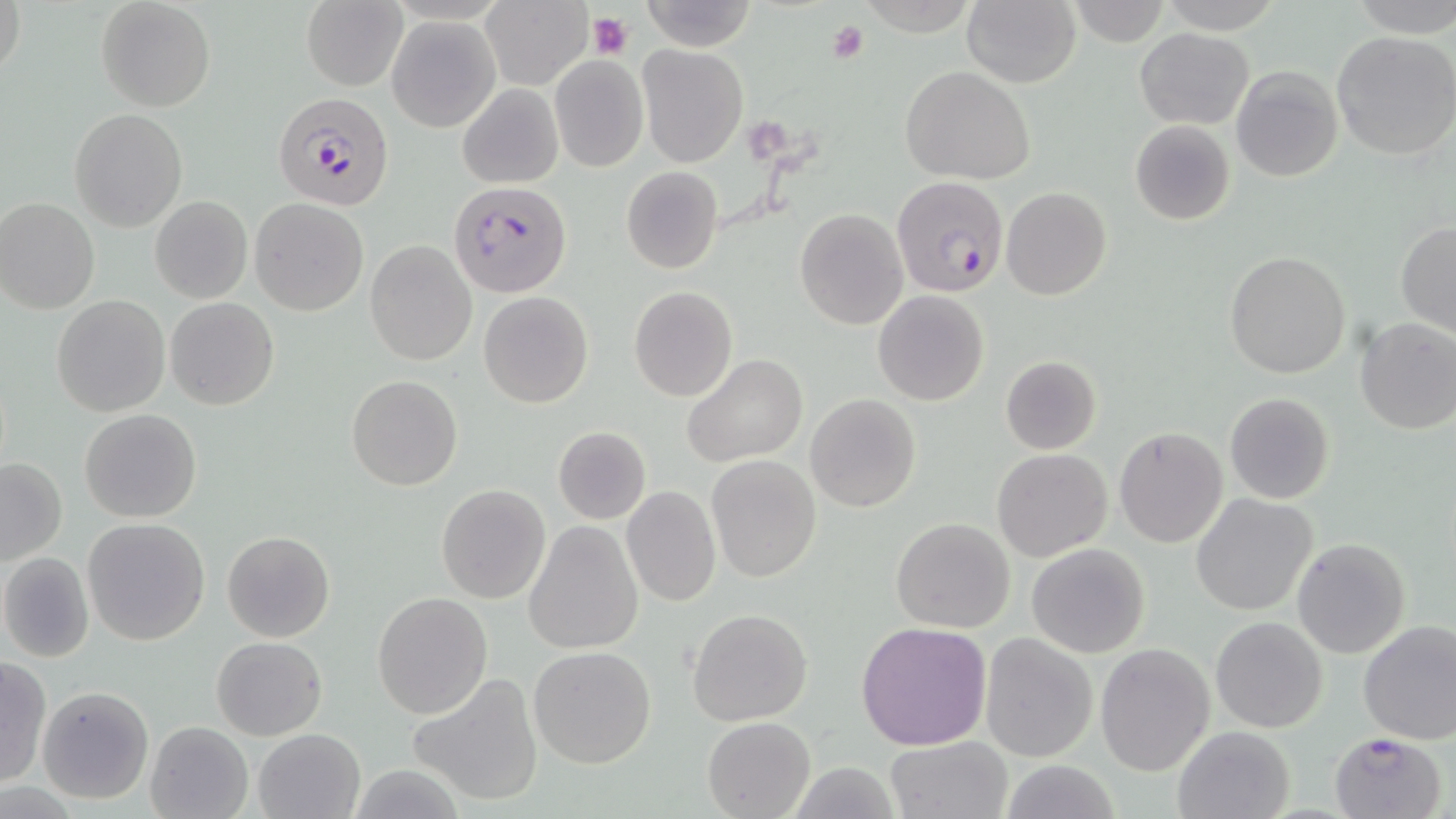

Summary:
  - Coordinate format: approximate bounding boxes as [x1, y1, x2, y2] in pixels
  - Uninfected red blood cell locations: [1, 0, 24, 85], [95, 0, 215, 112], [301, 0, 409, 91], [481, 0, 594, 90], [638, 0, 758, 51], [962, 0, 1081, 88], [1349, 0, 1456, 36], [1067, 1, 1171, 47], [389, 17, 499, 131], [1135, 28, 1254, 128], [1332, 31, 1456, 160], [638, 43, 748, 168], [549, 55, 648, 172], [902, 66, 1037, 185], [1231, 66, 1342, 183], [457, 84, 563, 188], [69, 109, 187, 232], [1130, 120, 1235, 225], [620, 166, 723, 274], [1001, 186, 1112, 300], [150, 195, 252, 303], [0, 197, 100, 314], [249, 198, 369, 316], [794, 208, 908, 330], [1396, 221, 1456, 335], [365, 240, 476, 365], [1225, 251, 1351, 377], [629, 286, 737, 401], [872, 290, 990, 406], [479, 292, 593, 408], [51, 294, 170, 417], [167, 298, 279, 411], [1355, 317, 1456, 435], [682, 354, 808, 467], [999, 356, 1102, 454], [347, 375, 461, 490], [1224, 393, 1334, 505], [806, 394, 921, 512], [79, 409, 202, 523], [552, 426, 652, 525], [1114, 428, 1227, 548], [992, 447, 1113, 562], [706, 455, 822, 584], [0, 457, 67, 565], [436, 484, 551, 603], [621, 485, 721, 607], [1191, 493, 1318, 615], [82, 518, 211, 646], [891, 518, 1015, 633], [523, 521, 643, 655], [221, 530, 336, 643], [1292, 537, 1411, 659], [1026, 542, 1150, 658], [0, 551, 95, 663], [372, 591, 492, 721], [687, 609, 813, 726], [1210, 616, 1328, 733], [1357, 619, 1456, 745], [856, 622, 992, 750], [980, 632, 1100, 762], [212, 636, 326, 739], [1095, 644, 1213, 774], [528, 645, 656, 768], [0, 657, 50, 788], [407, 676, 543, 807], [37, 685, 154, 805], [702, 716, 815, 818], [144, 720, 253, 819], [1171, 724, 1296, 819], [253, 729, 365, 818], [885, 735, 1015, 819], [999, 760, 1121, 818], [787, 762, 905, 819]
  - Platelet locations: [587, 11, 634, 59], [827, 21, 870, 64]
  - Plasmodium falciparum-infected red blood cell locations: [273, 90, 395, 210], [894, 178, 1009, 298], [451, 181, 571, 296], [1326, 730, 1448, 819]
  - Slide-level diagnosis: Plasmodium falciparum
  - Field of view: one of a larger specimen
  - Modality: light microscopy
  - Magnification: 1000x
  - Stain: May-Grünwald-Giemsa
  - Preparation: thin blood film
  - Image size: 1456×819 pixels